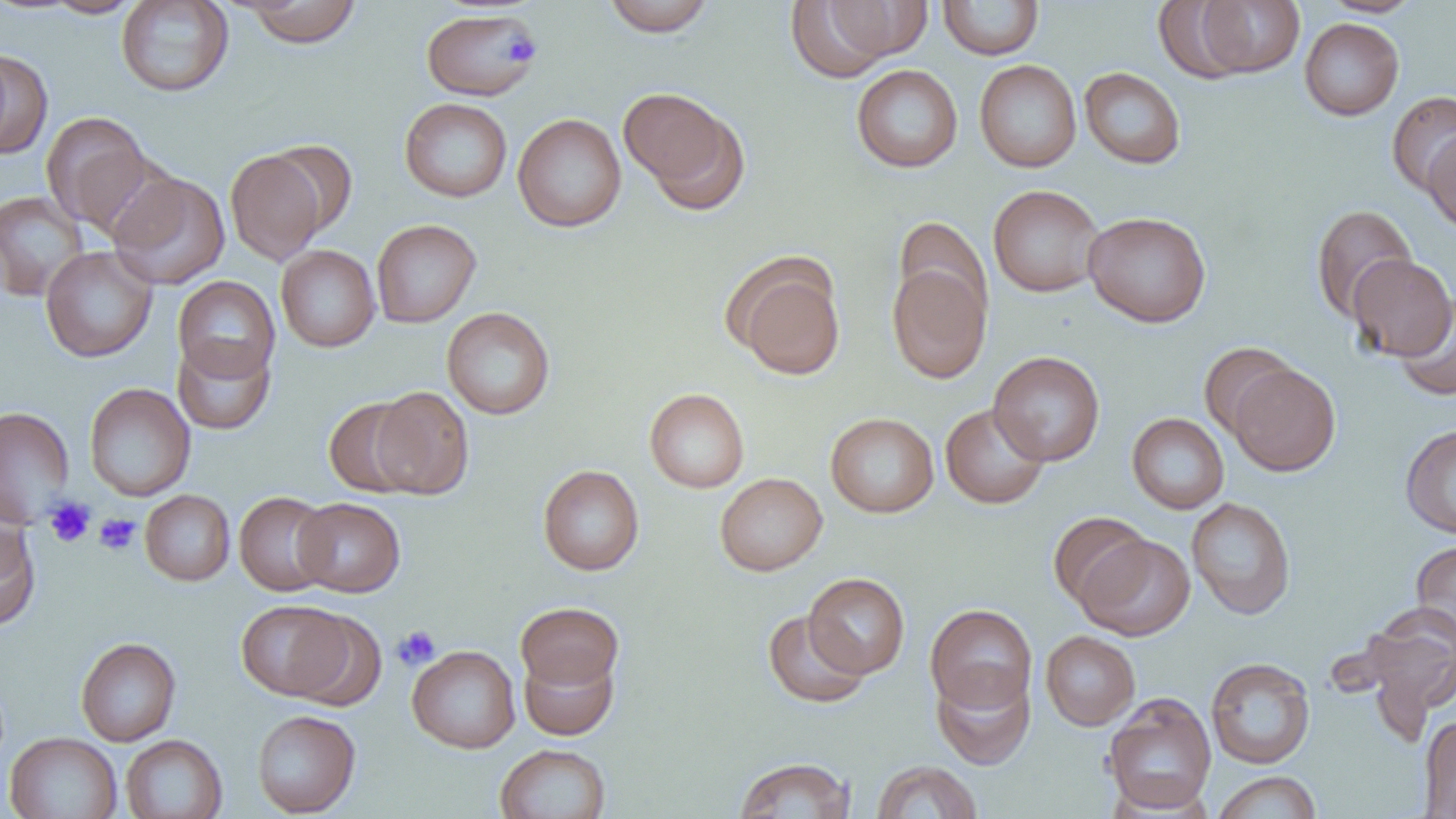

Approximate bounding boxes as (x1,y1)-(x2,y2) corner pairs in pixels. Uninfected red blood cell locations: (239,0)-(363,48), (602,0)-(715,36), (1321,0)-(1424,17), (41,1)-(146,18), (116,1)-(234,97), (782,1)-(920,80), (937,1)-(1044,60), (1191,1)-(1305,79), (421,8)-(541,101), (1299,17)-(1404,121), (0,48)-(52,159), (974,59)-(1082,173), (851,64)-(963,173), (1079,67)-(1186,169), (619,89)-(746,209), (1387,91)-(1456,196), (399,97)-(512,202), (41,112)-(154,234), (512,113)-(626,232), (1423,130)-(1456,233), (265,142)-(357,237), (226,149)-(328,264), (108,171)-(230,290), (988,184)-(1105,298), (0,190)-(88,301), (1311,204)-(1418,323), (1083,211)-(1211,327), (893,216)-(992,323), (371,219)-(482,328), (276,245)-(380,352), (40,246)-(157,363), (1347,255)-(1455,361), (727,256)-(846,381), (887,261)-(992,383), (173,276)-(280,383), (1393,294)-(1456,401), (442,307)-(556,420), (172,338)-(275,435), (1199,342)-(1300,440), (988,351)-(1105,466), (1229,363)-(1340,476), (84,383)-(195,501), (370,386)-(474,499), (644,388)-(749,493), (323,398)-(423,498), (940,403)-(1050,509), (0,405)-(75,528), (826,412)-(939,517), (1127,413)-(1229,514), (1400,424)-(1456,539), (537,464)-(645,576), (714,472)-(828,576), (140,490)-(235,585), (234,490)-(336,596), (293,497)-(406,597), (1186,497)-(1296,620), (1048,511)-(1152,612), (0,520)-(41,631), (1078,533)-(1194,641), (1411,540)-(1456,642), (804,572)-(910,678), (235,600)-(354,701), (515,601)-(623,691), (925,603)-(1037,713), (1359,603)-(1456,720), (285,610)-(387,711), (762,610)-(872,708), (1041,631)-(1140,730), (76,637)-(181,746), (407,645)-(520,753), (519,649)-(619,741), (1205,657)-(1316,769), (932,668)-(1035,770), (1102,692)-(1217,814), (252,709)-(361,817), (1419,715)-(1456,818), (4,732)-(122,819), (120,734)-(228,818), (495,743)-(611,819), (732,757)-(856,818), (871,760)-(982,819), (1212,771)-(1323,819). Platelet locations: (501,33)-(541,68), (45,496)-(95,548), (94,513)-(141,555), (392,626)-(441,670). Slide-level diagnosis: no evidence of blood parasites. Image is 1456×819 pixels. Thin blood film. Light microscopy. 1000x magnification. One field of a larger specimen.